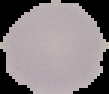

Summary:
  - Result: no malaria parasites detected
  - Preparation: thin blood film
  - Image size: 109×94 pixels
  - Image type: cell region segmented out of the field of view; surrounding area masked to black